State which parasite is depicted.
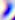

Toxoplasma gondii.

magnification = 400x
modality = photomicrograph